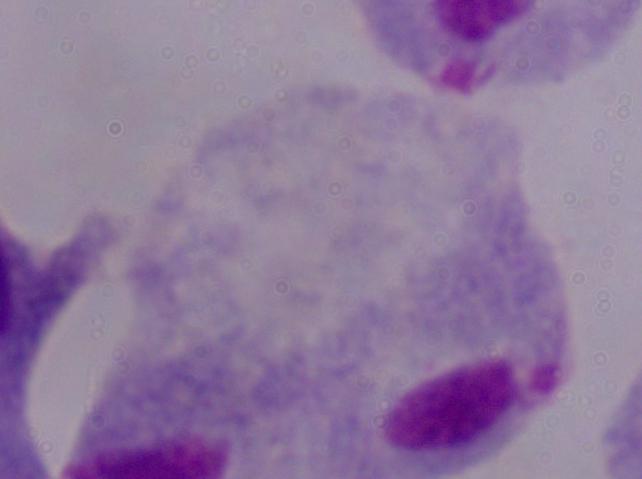
Captured at 1000x magnification. Photomicrograph. A trichomonad is shown.